Give the position of every Plasmodium parasite and every leukocyte.
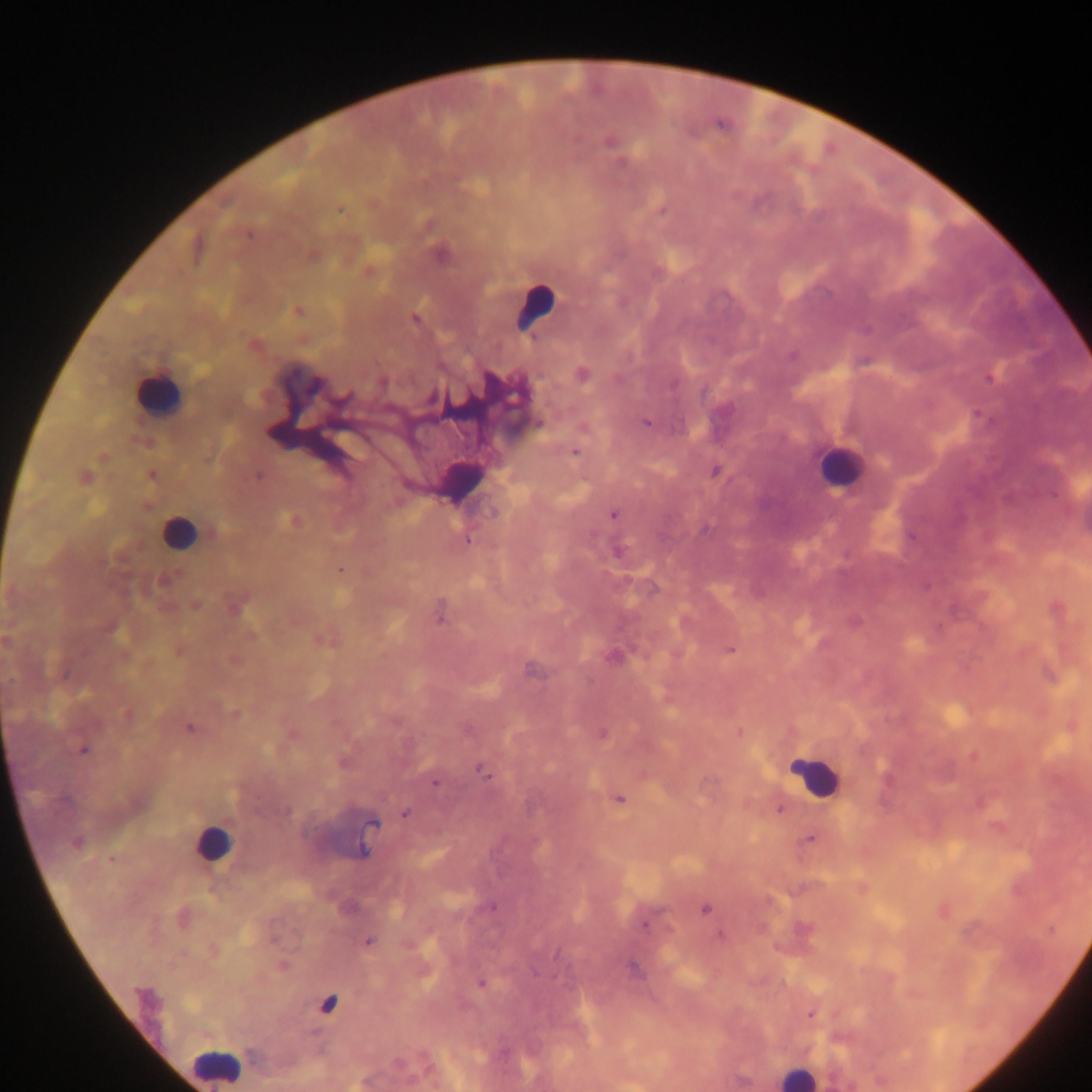
Approximate centers as {x, y} in pixels.
Plasmodium parasites: {610, 141}, {622, 163}, {339, 210}, {661, 211}, {248, 235}, {440, 254}, {312, 255}, {370, 272}, {658, 272}, {298, 311}, {415, 319}, {792, 356}, {582, 374}, {990, 377}, {382, 382}, {673, 384}, {316, 387}, {346, 398}, {431, 398}, {645, 423}, {539, 424}, {575, 452}, {103, 458}, {715, 471}, {152, 476}, {84, 477}, {258, 477}, {493, 513}, {613, 514}, {292, 521}, {466, 540}, {617, 551}, {340, 570}, {165, 580}, {196, 606}, {236, 609}, {440, 616}, {113, 629}, {324, 642}, {730, 649}, {615, 658}, {127, 714}, {235, 714}, {190, 728}, {739, 731}, {603, 733}, {83, 750}, {484, 772}, {435, 783}, {619, 799}, {66, 801}, {780, 810}, {286, 812}, {406, 813}, {372, 823}, {810, 839}, {77, 842}, {362, 850}, {110, 859}, {705, 908}, {644, 925}, {721, 935}, {369, 942}, {283, 966}, {633, 968}, {481, 984}, {145, 997}, {811, 1015}, {743, 1081}.
Leukocytes: {535, 306}, {157, 393}, {839, 466}, {459, 476}, {178, 532}, {816, 777}, {211, 845}, {327, 1003}, {216, 1065}, {796, 1076}.

{
  "capture": "mobile-phone photograph through a microscope",
  "field_of_view": "single",
  "preparation": "thick blood smear",
  "image_size": "1092×1092 pixels",
  "country": "Ghana"
}